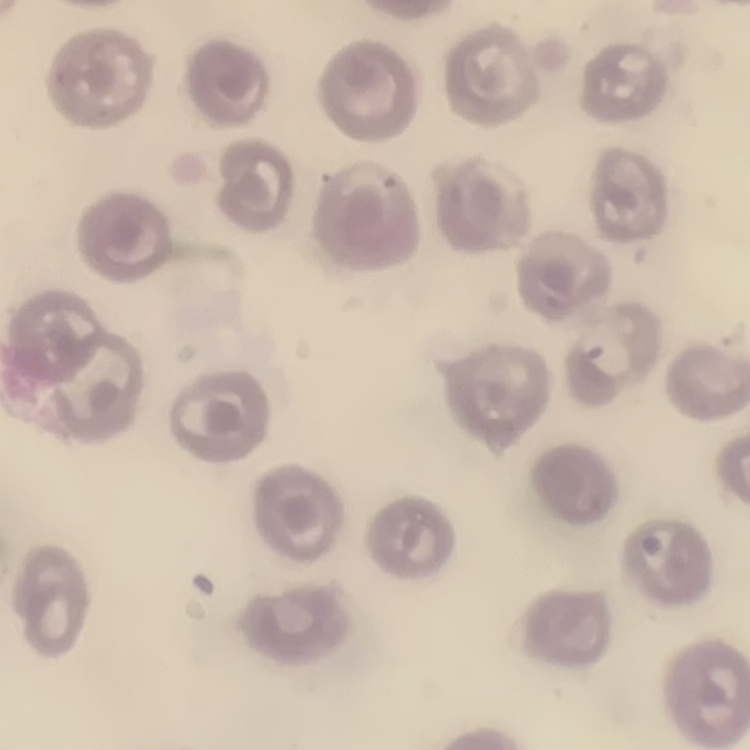 The red blood cells show no rouleaux formation. One tile cut from a larger photomicrograph. Thin peripheral smear. Stained with either Field's or Giemsa.